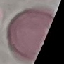
Summary:
  - Malaria status: uninfected
  - Stain: Giemsa
  - Preparation: thin smear
  - Capture: smartphone camera at the microscope eyepiece
  - Image type: cell patch, automatically extracted from a larger field of view and resized to 64 × 64 pixels